Give the extent of all white blood cells.
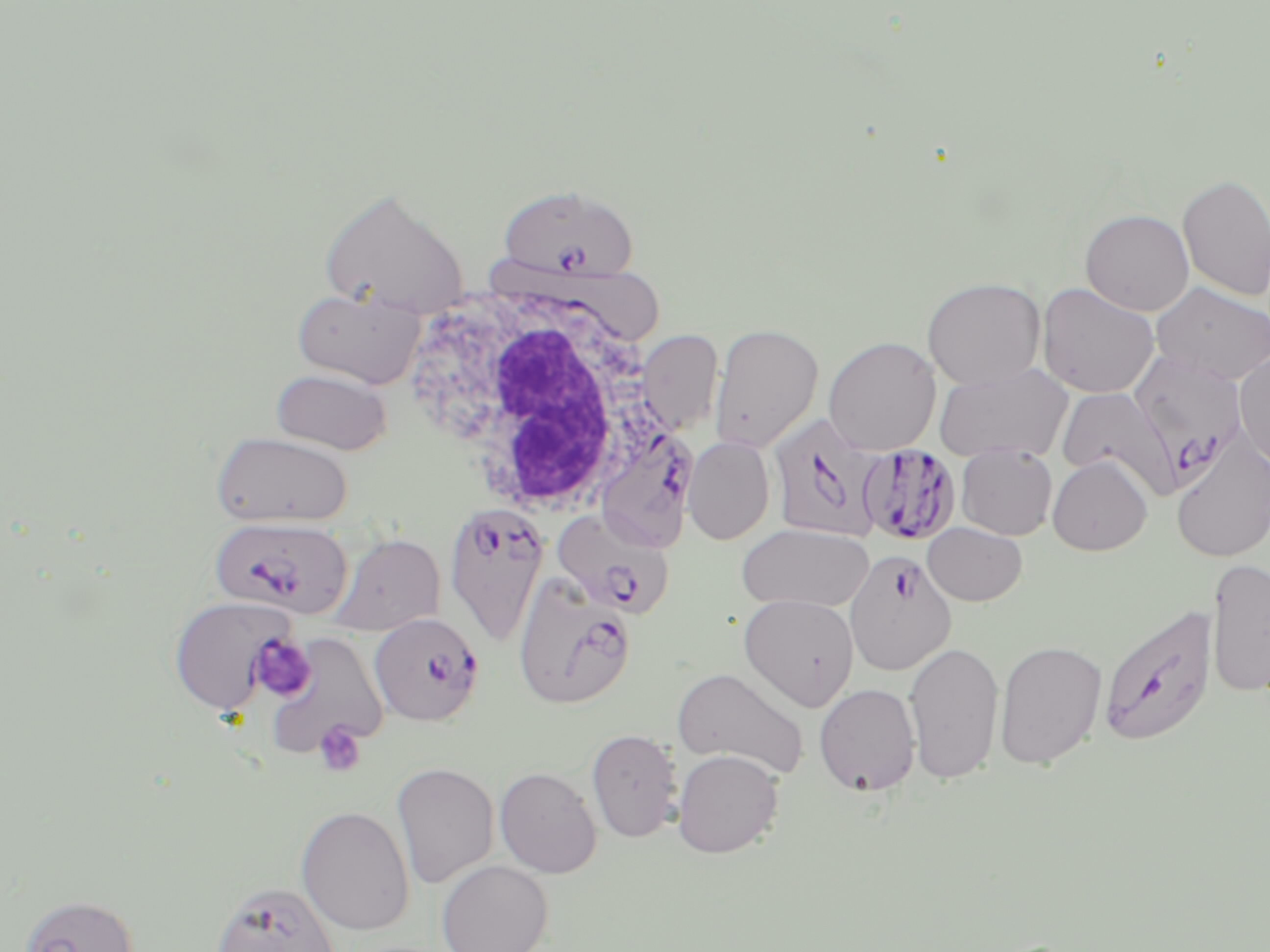

Approximate bounding boxes as (x1, y1, x2, y2) in pixels.
White blood cells: (407, 271, 680, 525).

Summary:
  - Platelet locations: (252, 635, 313, 700), (315, 723, 365, 776)
  - Plasmodium falciparum-infected red blood cell locations: (496, 183, 641, 282), (1137, 357, 1242, 489), (768, 413, 888, 544), (604, 431, 697, 557), (859, 442, 961, 543), (444, 502, 550, 648), (552, 509, 674, 620), (210, 516, 353, 619), (844, 550, 956, 675), (514, 573, 636, 710), (1097, 601, 1218, 748), (369, 612, 483, 726)
  - Uninfected red blood cell locations: (1177, 173, 1270, 302), (319, 187, 469, 316), (1080, 208, 1194, 316), (922, 277, 1046, 389), (1037, 282, 1160, 399), (1151, 283, 1270, 385), (292, 287, 425, 389), (709, 323, 823, 452), (637, 329, 723, 435), (823, 336, 941, 455), (1234, 348, 1270, 470), (933, 363, 1073, 463), (271, 368, 392, 455), (1055, 386, 1179, 498), (211, 432, 352, 528), (683, 436, 775, 544), (1170, 438, 1270, 562), (956, 444, 1057, 540), (1047, 455, 1153, 556), (922, 522, 1027, 606), (738, 523, 874, 613), (329, 533, 446, 636), (1205, 557, 1270, 698), (738, 594, 859, 711), (168, 596, 298, 715), (263, 633, 390, 759), (994, 639, 1107, 769), (904, 640, 1004, 786), (672, 667, 809, 780), (814, 683, 921, 796), (586, 728, 683, 843), (672, 749, 784, 858), (392, 760, 499, 888), (495, 766, 602, 878), (296, 805, 415, 936), (436, 859, 553, 952), (210, 880, 343, 952), (18, 893, 139, 952)
  - Slide-level diagnosis: Plasmodium falciparum
  - Image size: 1270×952 pixels
  - Stain: May-Grünwald-Giemsa
  - Modality: optical microscopy
  - Magnification: 1000x
  - Field of view: single
  - Preparation: thin blood film